Locate and identify every blood parasite.
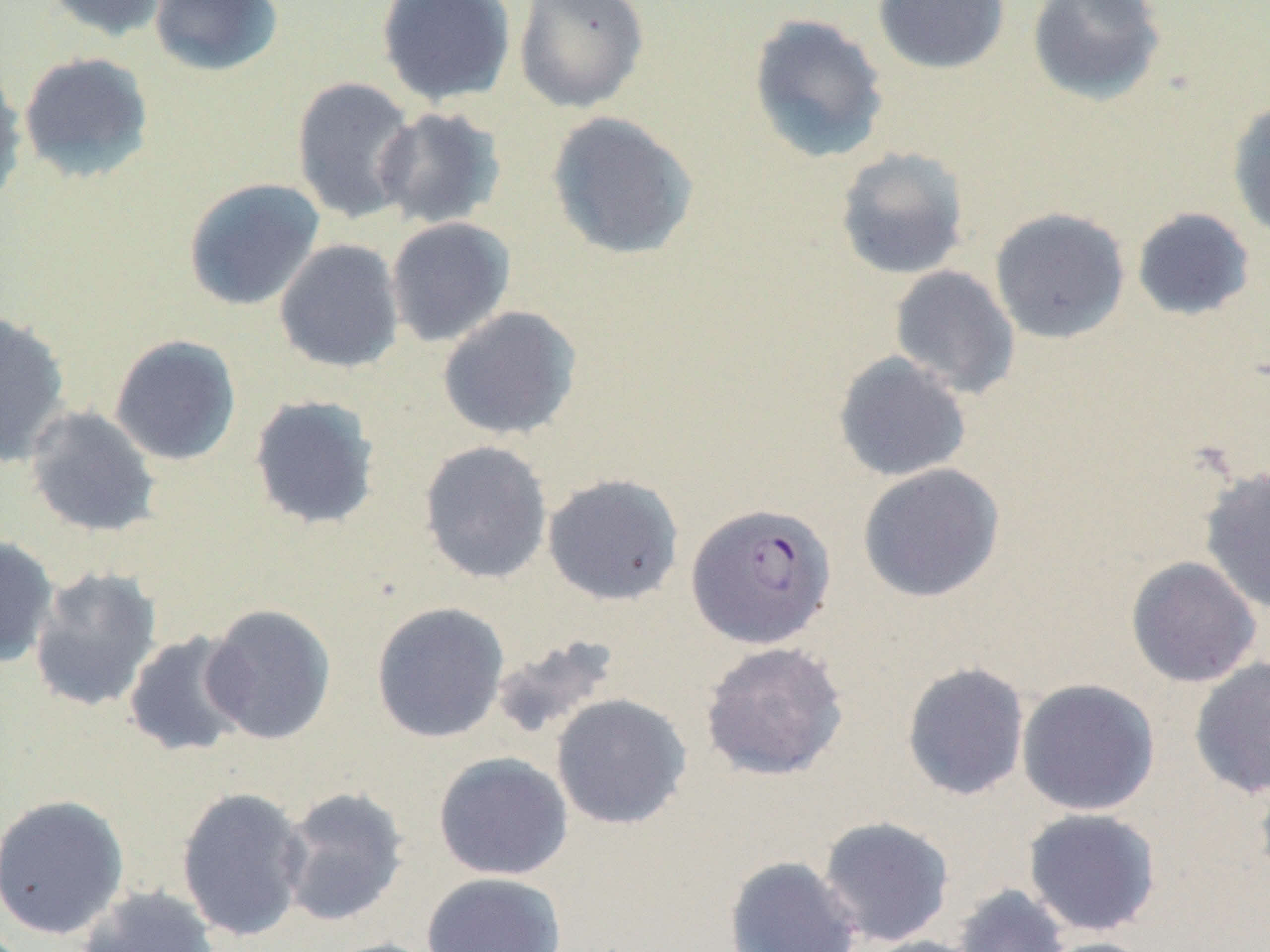
Approximate bounding boxes as (x1,y1)-(x2,y2) corner pairs in pixels.
Plasmodium falciparum-infected red blood cells: (685,503)-(836,649).
No Plasmodium ovale, Plasmodium malariae, Plasmodium vivax, Babesia divergens, or Trypanosoma brucei observed.

Summary:
  - Uninfected red blood cell locations: (41,0)-(172,41), (149,0)-(284,76), (376,0)-(517,108), (513,0)-(650,114), (872,0)-(1010,75), (1027,0)-(1167,107), (747,13)-(890,165), (17,51)-(155,183), (0,63)-(27,210), (291,76)-(419,224), (1227,98)-(1270,242), (373,107)-(506,230), (546,111)-(699,262), (834,146)-(970,280), (183,177)-(325,311), (989,207)-(1131,344), (1131,207)-(1256,322), (385,217)-(516,348), (273,239)-(405,374), (889,265)-(1020,400), (437,305)-(582,441), (0,311)-(72,467), (108,334)-(242,466), (833,351)-(972,483), (247,394)-(382,532), (24,404)-(161,538), (418,440)-(553,584), (857,463)-(1005,603), (1199,466)-(1270,616), (542,473)-(685,607), (0,535)-(59,668), (1125,556)-(1263,688), (28,566)-(163,713), (371,601)-(510,743), (200,602)-(337,745), (122,630)-(253,758), (489,634)-(620,742), (699,640)-(850,782), (1188,656)-(1270,799), (900,661)-(1031,801), (1016,678)-(1160,816), (551,693)-(692,830), (433,751)-(574,880), (1253,770)-(1270,887), (175,785)-(311,942), (278,786)-(410,928), (0,793)-(131,940), (1022,807)-(1163,938), (817,815)-(955,947), (723,855)-(863,952), (421,871)-(567,952), (951,884)-(1072,952), (75,885)-(223,952), (856,936)-(989,952), (1034,936)-(1160,952), (318,937)-(445,952)
  - Slide-level diagnosis: Plasmodium falciparum
  - Image size: 1270×952 pixels
  - Field of view: single
  - Modality: light microscopy
  - Preparation: thin blood film
  - Stain: May-Grünwald-Giemsa
  - Magnification: 1000x